Point out every Plasmodium parasite.
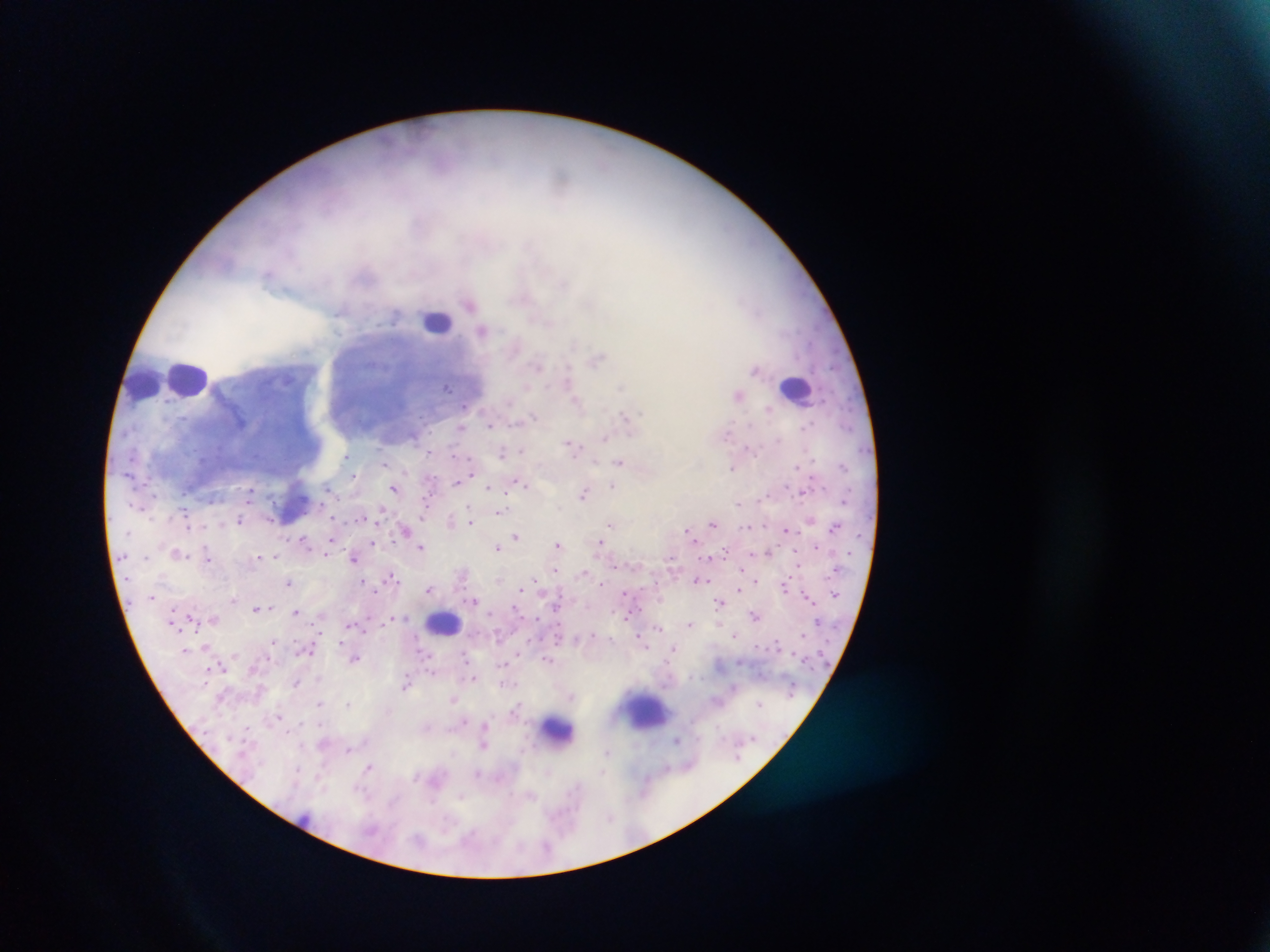

Approximate centers as (x, y) in pixels.
Plasmodium parasites: (469, 303), (482, 330), (597, 359), (538, 365), (568, 379), (447, 387), (465, 407), (769, 409), (533, 415), (626, 416), (808, 424), (489, 425), (462, 428), (728, 432), (604, 439), (777, 440), (570, 444), (748, 448), (522, 450), (430, 452), (502, 453), (345, 456), (620, 462), (384, 463), (796, 466), (842, 466), (732, 467), (354, 475), (458, 481), (520, 484), (489, 487), (612, 487), (327, 488), (394, 489), (251, 492), (584, 493), (766, 495), (739, 503), (425, 507), (501, 511), (380, 513), (241, 520), (451, 521), (469, 521), (611, 524), (712, 524), (188, 526), (834, 527), (405, 529), (786, 529), (687, 530), (516, 536), (304, 540), (373, 543), (558, 544), (601, 544), (421, 546), (817, 546), (498, 548), (206, 550), (177, 553), (769, 553), (326, 554), (275, 556), (207, 557), (258, 557), (265, 557), (146, 558), (354, 558), (555, 570), (741, 570), (583, 573), (392, 577), (698, 580), (364, 581), (534, 581), (755, 582), (288, 583), (601, 585), (784, 586), (429, 589), (739, 590), (626, 593), (151, 596), (808, 598), (233, 599), (474, 600), (719, 602), (556, 607), (256, 608), (516, 609), (295, 612), (755, 615), (626, 616), (690, 624), (658, 628), (736, 634), (593, 635), (272, 641), (673, 649), (428, 655), (356, 658), (465, 658), (548, 659), (503, 664), (223, 669), (474, 678), (318, 679), (297, 683), (406, 684), (571, 695), (453, 699), (319, 703), (760, 703), (348, 704), (279, 716), (463, 721), (484, 726), (427, 727), (246, 728), (677, 740), (483, 745), (349, 750), (608, 751), (368, 767), (297, 769), (549, 772), (602, 773), (477, 774), (576, 787), (360, 790), (531, 795), (462, 796), (610, 817), (471, 834).

Leukocyte locations: (437, 321), (187, 379), (143, 382), (797, 388), (295, 506), (444, 623), (650, 711), (557, 731). Mobile-phone photograph taken through the microscope. Thick blood smear. Image is 1270×952 pixels. Collected in Ghana. One field of view.